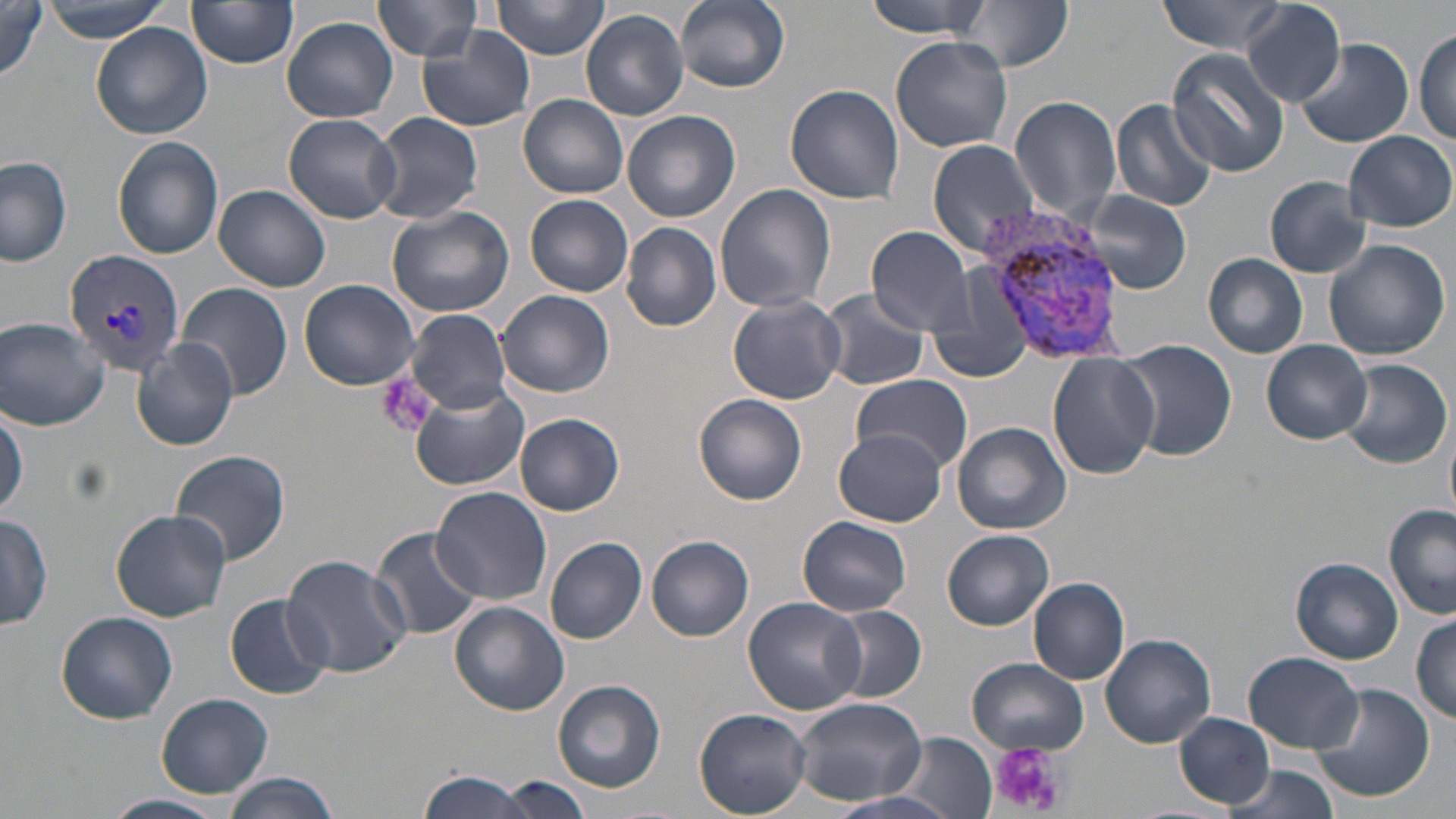

slide_level_diagnosis: Plasmodium vivax
uninfected_red_blood_cell_locations: 'approximate bounding boxes as (x1, y1, x2, y2) in pixels: (43, 0, 173, 41), (186, 0, 299, 70), (372, 0, 484, 61), (493, 0, 610, 60), (674, 0, 789, 91), (864, 0, 992, 38), (954, 0, 1072, 73), (1157, 0, 1291, 57), (0, 1, 46, 84), (1241, 2, 1347, 108), (581, 10, 689, 120), (282, 16, 398, 123), (90, 22, 213, 140), (418, 25, 536, 131), (1413, 30, 1455, 145), (890, 36, 1015, 153), (1295, 39, 1412, 148), (1166, 48, 1290, 177), (784, 84, 904, 204), (518, 94, 629, 198), (1008, 94, 1122, 218), (1111, 98, 1219, 213), (624, 110, 739, 222), (284, 112, 403, 222), (369, 112, 483, 223), (1341, 129, 1454, 232), (113, 136, 223, 260), (927, 137, 1043, 255), (0, 157, 72, 267), (1264, 175, 1374, 278), (214, 185, 331, 292), (714, 185, 836, 317), (1072, 188, 1194, 294), (526, 195, 633, 297), (385, 205, 514, 318), (622, 221, 721, 332), (868, 225, 975, 335), (1323, 240, 1450, 361), (1203, 252, 1310, 359), (298, 279, 420, 391), (177, 283, 293, 401), (497, 290, 615, 397), (813, 291, 932, 391), (728, 294, 846, 403), (405, 309, 511, 414), (0, 318, 110, 429), (927, 327, 1032, 376), (133, 338, 238, 450), (1115, 338, 1238, 464), (1263, 340, 1373, 445), (1047, 353, 1158, 479), (1341, 359, 1451, 470), (850, 374, 974, 472), (409, 385, 528, 492), (984, 385, 1137, 512), (695, 395, 807, 504), (1, 405, 27, 520), (1444, 413, 1456, 525), (515, 414, 623, 516), (952, 422, 1072, 535), (833, 430, 948, 526), (170, 450, 291, 564), (432, 487, 555, 607), (1384, 507, 1456, 621), (112, 509, 231, 621), (1, 512, 53, 631), (798, 515, 913, 617), (369, 526, 484, 640), (943, 530, 1054, 629), (646, 535, 754, 641), (545, 537, 647, 643), (283, 553, 412, 679), (1292, 558, 1403, 664), (1028, 576, 1130, 685), (225, 594, 334, 700), (743, 596, 867, 715), (449, 603, 568, 716), (826, 605, 927, 703), (56, 611, 177, 724), (1411, 614, 1455, 724), (1100, 633, 1215, 747), (1243, 652, 1365, 753), (966, 658, 1089, 754), (553, 680, 667, 794), (1310, 682, 1435, 804), (156, 692, 273, 799), (791, 696, 929, 804), (695, 709, 812, 816), (1174, 712, 1275, 807), (887, 734, 999, 816), (1224, 765, 1343, 819), (418, 770, 542, 818), (221, 774, 341, 818), (499, 776, 592, 817), (823, 790, 967, 819), (103, 794, 229, 819)'
platelet_locations: 'approximate bounding boxes as (x1, y1, x2, y2) in pixels: (377, 371, 436, 439), (990, 743, 1066, 818)'
magnification: 1000x
plasmodium_vivax_infected_red_blood_cell_locations: 'approximate bounding boxes as (x1, y1, x2, y2) in pixels: (980, 211, 1124, 359), (63, 251, 190, 373)'
stain: May-Grünwald-Giemsa
image_size: 1456×819 pixels
modality: optical microscopy
preparation: thin blood smear
field_of_view: single